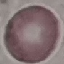

Malaria status: uninfected. Acquired by smartphone through the microscope eyepiece. Automatically extracted cell patch, resized to 64 × 64 pixels. Giemsa-stained preparation. Thin smear of blood.